Locate and identify every blood parasite.
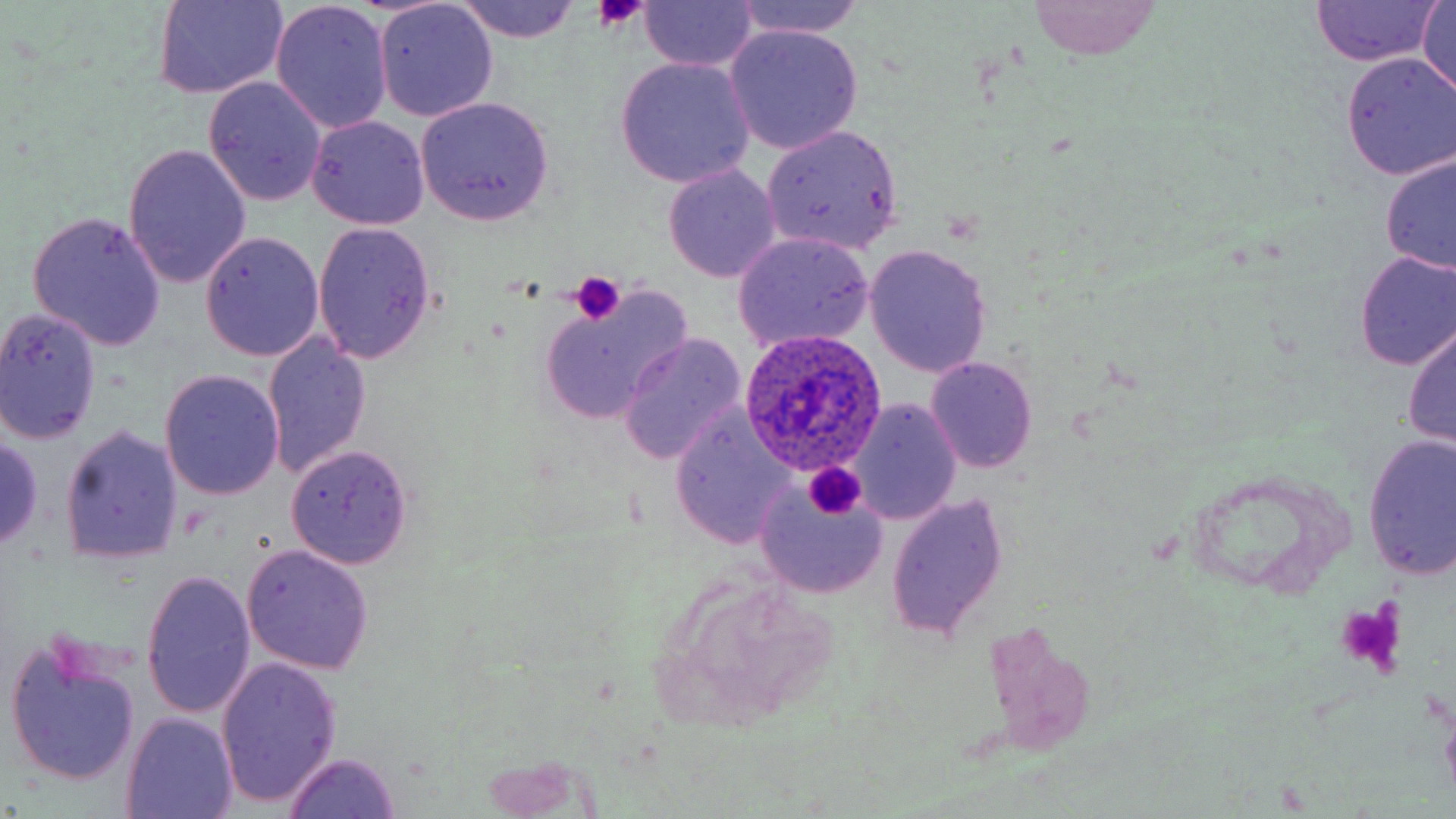
Approximate bounding boxes as [x1, y1, x2, y2] in pixels.
Plasmodium ovale-infected red blood cells: [737, 330, 889, 477].
No Plasmodium falciparum, Plasmodium malariae, Plasmodium vivax, Babesia divergens, or Trypanosoma brucei observed.

Summary:
  - Platelet locations: [593, 0, 644, 33], [569, 271, 626, 323], [802, 462, 866, 519], [1334, 597, 1407, 679]
  - Uninfected red blood cell locations: [153, 0, 287, 98], [1309, 0, 1444, 67], [1419, 0, 1455, 97], [452, 1, 583, 43], [636, 1, 760, 72], [1028, 1, 1161, 59], [374, 2, 498, 121], [727, 2, 875, 42], [271, 3, 393, 135], [725, 24, 864, 154], [1339, 52, 1456, 180], [614, 57, 755, 187], [203, 78, 327, 207], [414, 97, 556, 227], [306, 116, 430, 231], [760, 124, 904, 255], [124, 144, 252, 290], [1380, 152, 1456, 276], [662, 163, 780, 284], [28, 212, 166, 350], [312, 222, 437, 365], [732, 231, 874, 352], [200, 233, 326, 360], [866, 244, 992, 378], [1353, 250, 1455, 370], [537, 290, 692, 424], [0, 309, 102, 445], [1402, 316, 1456, 451], [262, 333, 373, 482], [620, 336, 747, 465], [926, 358, 1037, 472], [160, 370, 284, 501], [848, 399, 961, 524], [668, 411, 793, 548], [59, 424, 183, 562], [0, 433, 46, 549], [1361, 433, 1456, 585], [286, 444, 413, 567], [755, 488, 888, 598], [885, 491, 1009, 643], [241, 545, 375, 674], [142, 569, 257, 722], [5, 638, 143, 789], [217, 657, 342, 811], [121, 714, 237, 819], [282, 755, 403, 818]
  - Slide-level diagnosis: Plasmodium ovale
  - Preparation: thin blood film
  - Field of view: single
  - Image size: 1456×819 pixels
  - Magnification: 1000x
  - Stain: May-Grünwald-Giemsa
  - Modality: optical microscopy